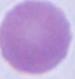

1000x magnification. A red blood cell is shown. Photomicrograph.